Report the malaria status of this cell.
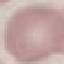

It is uninfected.

preparation = thin smear
image type = automatically extracted cell patch, resized to 64 × 64 pixels
capture = smartphone camera at the microscope eyepiece
stain = Giemsa